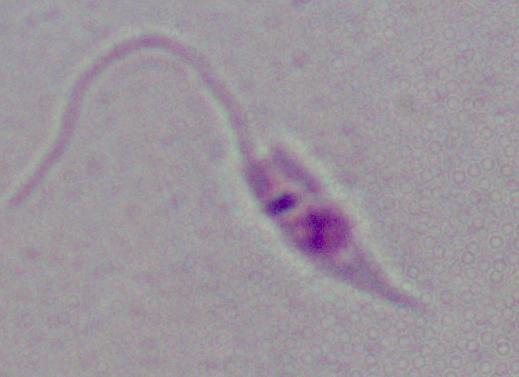

A Leishmania parasite is shown. 1000x magnification. Micrograph.